Report the malaria status of this cell.
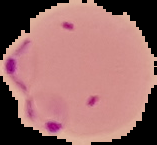
Parasitized.

Cell region segmented out of the field of view; the surrounding area is masked to black. From a thin blood film. Image is 157×145 pixels.